Describe the morphology of the red blood cells.
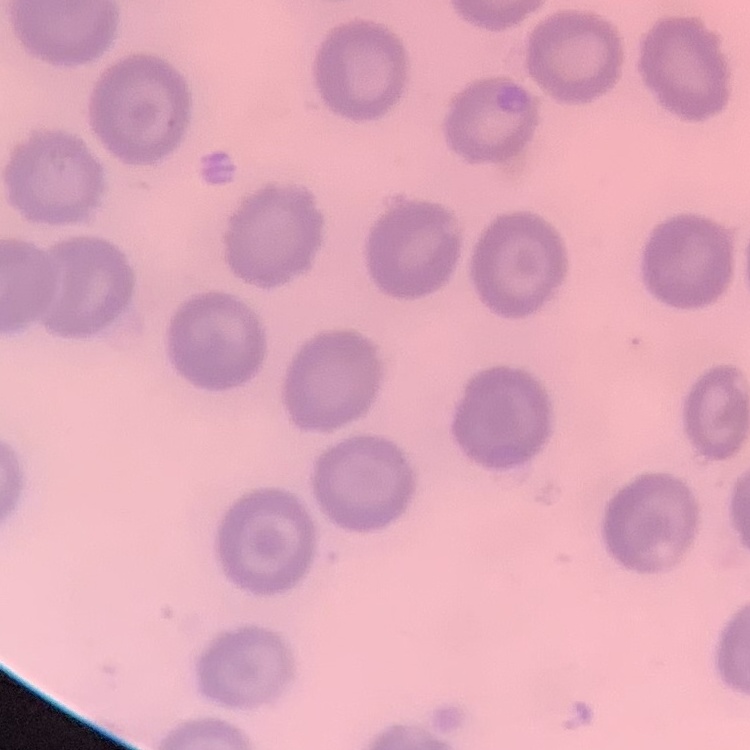

No rouleaux formation.

Stained with either Field's or Giemsa. Thin peripheral smear. Square crop of a larger photomicrograph.